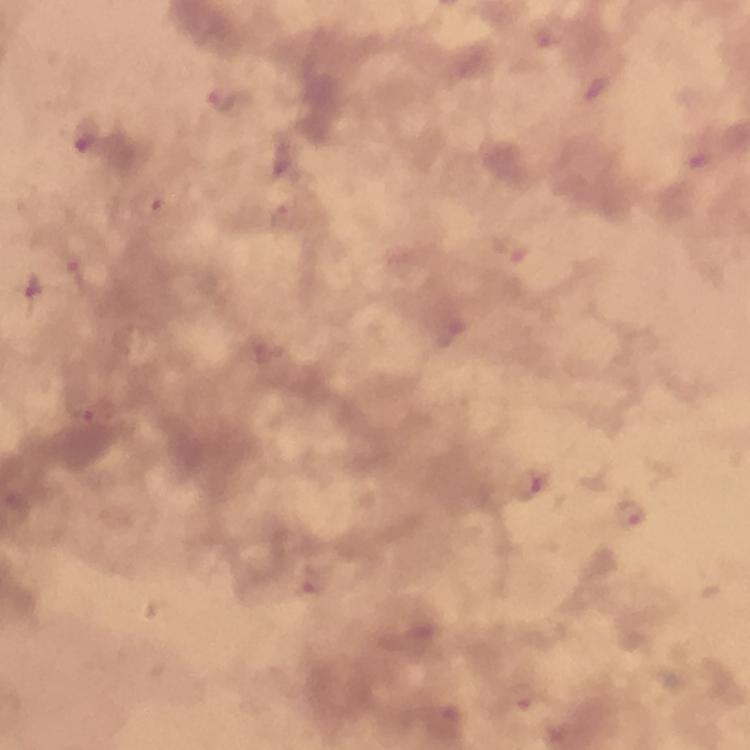 Approximate centers as {x, y} in pixels. Plasmodium parasite locations: {545, 37}, {224, 100}, {87, 137}, {279, 159}, {151, 201}, {283, 218}, {511, 247}, {74, 272}, {29, 289}, {451, 335}, {94, 417}, {530, 487}, {630, 513}, {313, 579}, {520, 700}. Photographed through the microscope with a smartphone camera. Thick blood film. Image is 750×750 pixels. Giemsa-stained preparation. 100x magnification. Immersion oil applied. From a diagnostic examination for malaria. Cropped region of a single field of view.